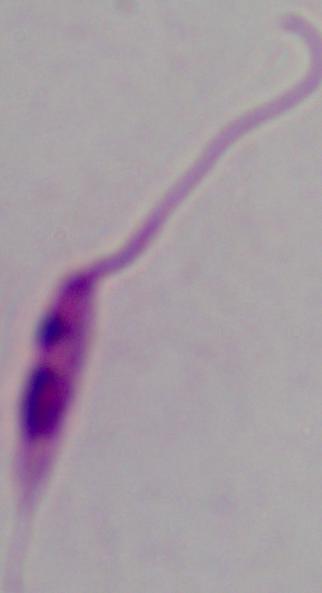
modality: photomicrograph
identification: Leishmania
magnification: 1000x